Name the parasite shown.
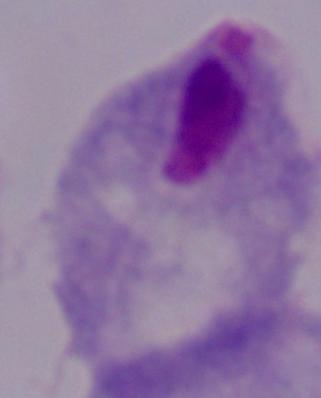
This is a trichomonad.

Summary:
  - Modality: micrograph
  - Magnification: 1000x